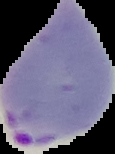
Image is 115×154 pixels. Segmented cell region on a black background. Malaria status: parasitized. From a thin blood film.